Identify the parasite.
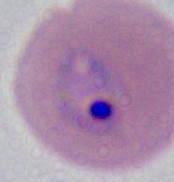

This is Plasmodium.

modality: photomicrograph
magnification: 400x or 1000x